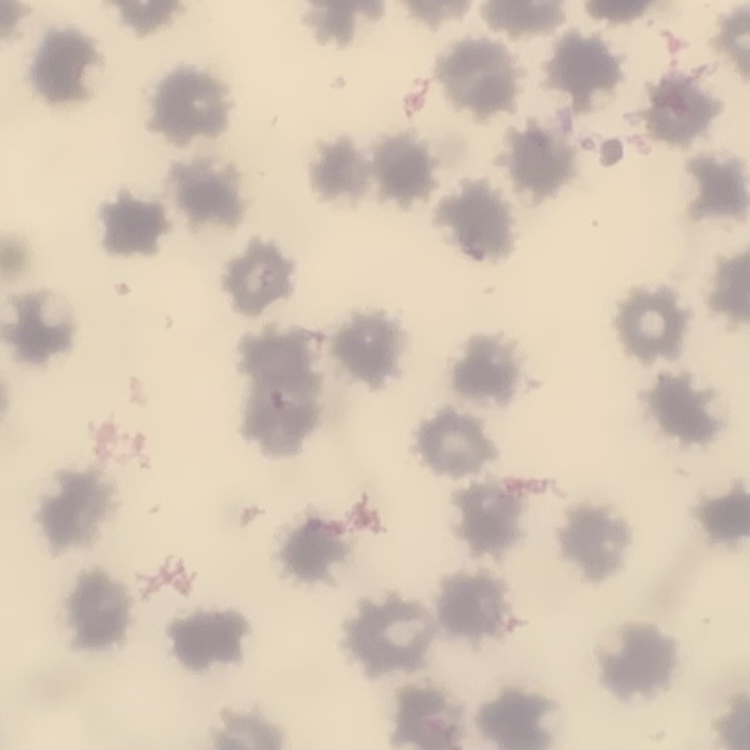

red_blood_cell_morphology: no rouleaux formation
stain: Field's or Giemsa
image_type: square crop of a larger photomicrograph
preparation: thin blood smear